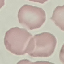
result: no malaria parasites seen
image_type: cell patch, automatically extracted from a larger field of view and resized to 64 × 64 pixels
stain: Giemsa
preparation: thin blood smear
capture: smartphone through the microscope eyepiece